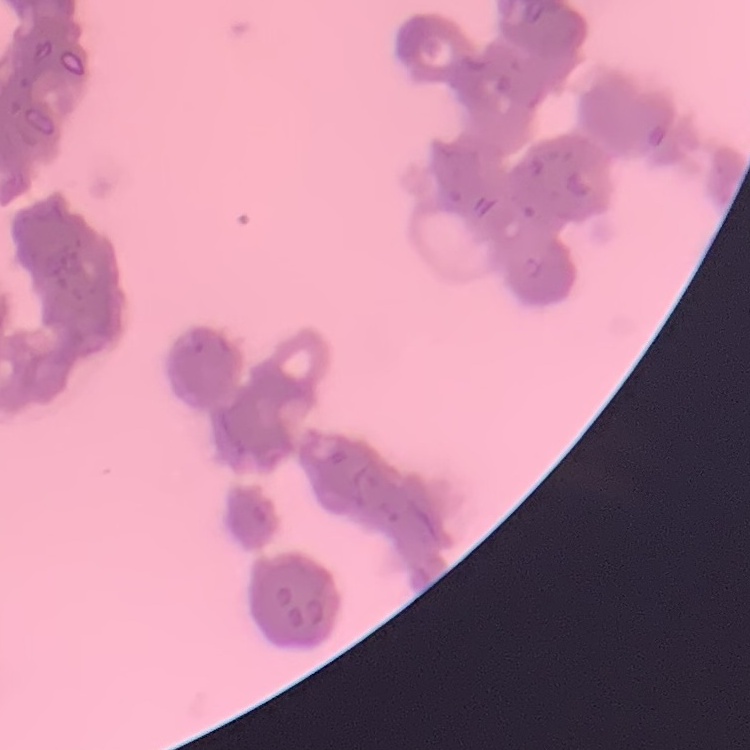 The erythrocytes exhibit rouleaux formation. Stained with either Field's or Giemsa. One tile cut from a larger photomicrograph. Thin blood film.